Classify this cell by malaria status.
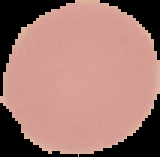
It is uninfected.

preparation = thin blood smear
image type = segmented cell region on a black background
image size = 160×157 pixels